Assess this cell for malaria.
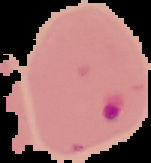

Parasitized.

Summary:
  - Image type: segmented cell region with the area outside set to black
  - Preparation: thin blood smear
  - Image size: 151×163 pixels